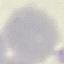
Summary:
  - Malaria status: uninfected
  - Preparation: thin smear
  - Stain: Giemsa
  - Image type: cell patch, automatically extracted from a larger field of view and resized to 64 × 64 pixels
  - Capture: smartphone camera at the microscope eyepiece